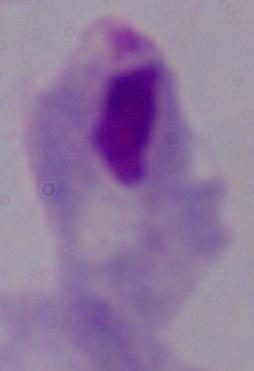

Summary:
  - Magnification: 1000x
  - Modality: photomicrograph
  - Identification: trichomonad